Comment on the morphology of the erythrocytes.
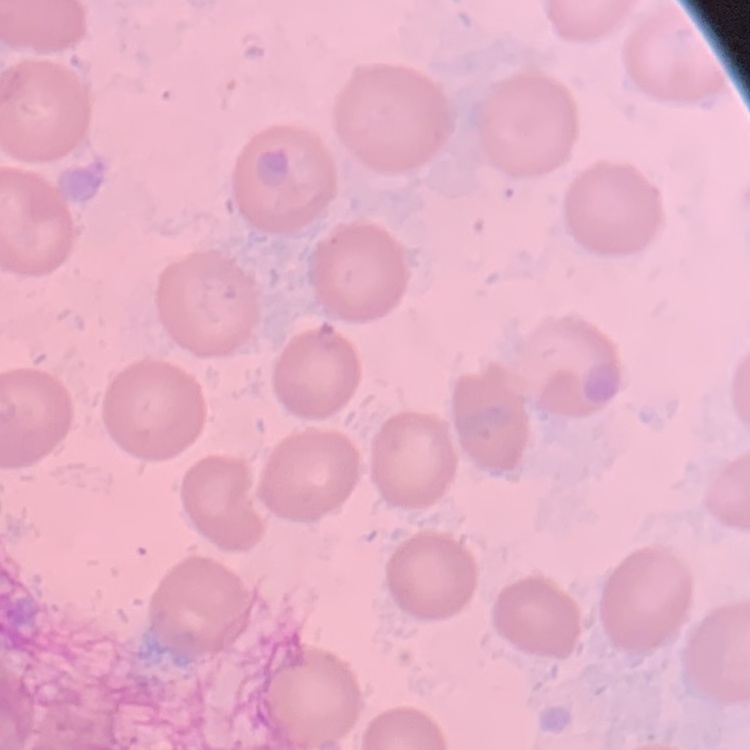

No rouleaux formation.

Square crop of a larger photomicrograph. Field's or Giemsa stain. Thin blood smear.